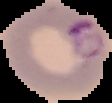 Segmented cell region on a black background. From a thin blood film. Image is 112×103 pixels. Result: Plasmodium parasites identified.